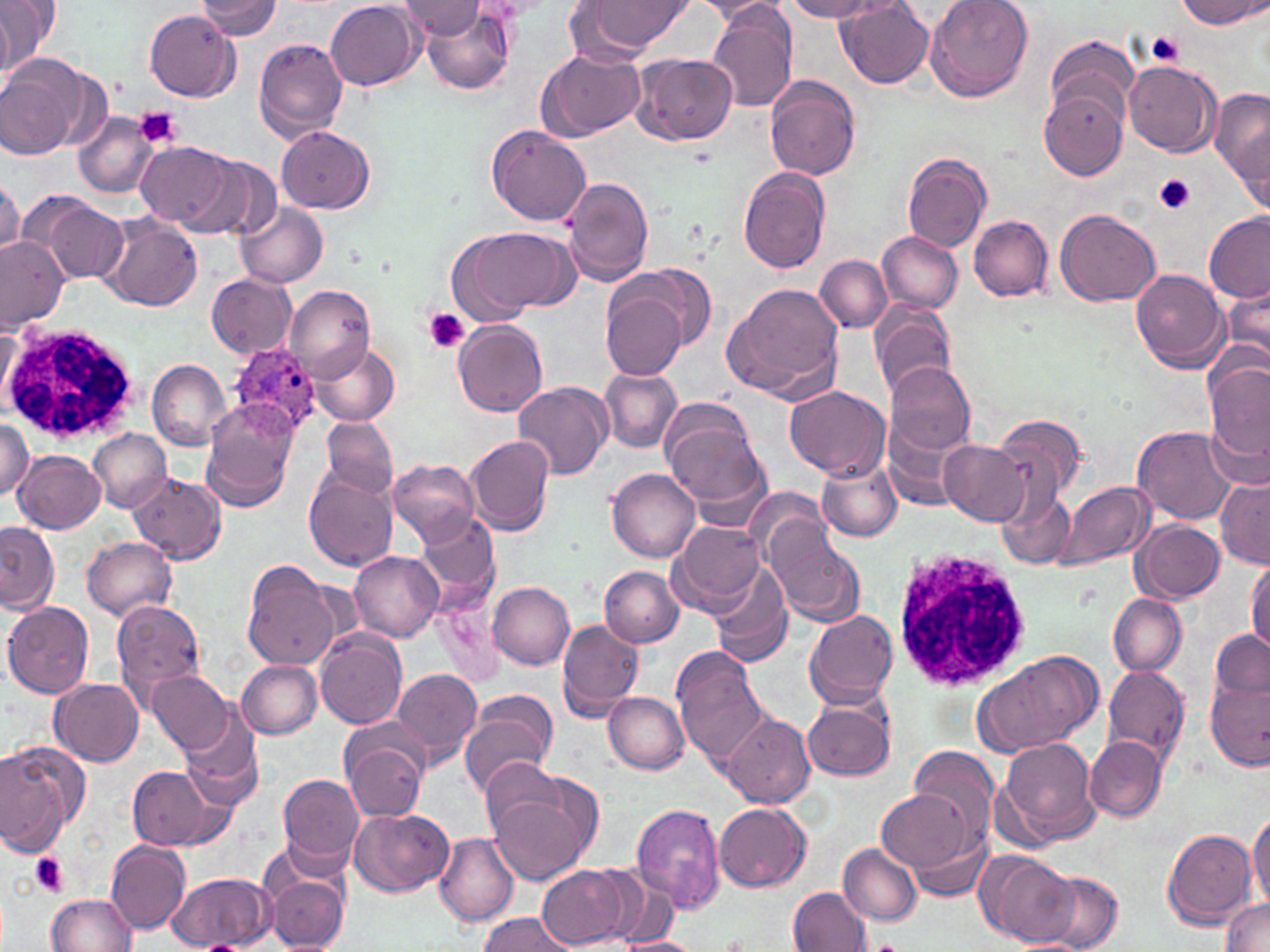

Summary:
  - Coordinate format: approximate bounding boxes as [x1, y1, x2, y2] in pixels
  - Platelet locations: [1145, 31, 1183, 68], [135, 107, 181, 150], [1154, 174, 1196, 215], [423, 308, 470, 353], [29, 852, 70, 897]
  - Plasmodium ovale-infected red blood cell locations: [226, 342, 323, 438]
  - White blood cell locations: [0, 321, 141, 444], [889, 547, 1034, 692]
  - Uninfected red blood cell locations: [0, 0, 58, 78], [196, 0, 282, 39], [325, 0, 421, 89], [586, 0, 694, 53], [693, 0, 787, 24], [784, 0, 887, 21], [835, 0, 935, 88], [925, 0, 1033, 102], [1176, 0, 1267, 30], [400, 1, 485, 39], [420, 5, 513, 96], [707, 5, 798, 114], [145, 11, 240, 101], [1043, 35, 1138, 126], [253, 37, 348, 144], [536, 49, 645, 141], [632, 52, 738, 145], [1, 56, 84, 158], [1124, 60, 1220, 157], [766, 75, 861, 179], [1212, 85, 1270, 197], [1039, 86, 1128, 180], [73, 111, 158, 198], [487, 125, 592, 227], [277, 127, 375, 213], [137, 141, 237, 231], [901, 153, 991, 252], [198, 156, 283, 241], [738, 166, 831, 274], [562, 175, 655, 287], [0, 179, 23, 259], [33, 196, 127, 284], [235, 203, 327, 289], [1055, 208, 1161, 307], [1202, 212, 1269, 304], [100, 215, 203, 310], [969, 215, 1053, 301], [451, 228, 558, 326], [878, 230, 962, 314], [0, 238, 69, 328], [816, 255, 891, 331], [636, 263, 714, 350], [1132, 269, 1228, 374], [206, 273, 296, 358], [723, 282, 847, 400], [283, 285, 374, 383], [601, 285, 688, 381], [1219, 285, 1270, 374], [869, 300, 957, 402], [454, 319, 548, 419], [0, 325, 19, 411], [310, 342, 400, 426], [146, 359, 230, 450], [884, 361, 976, 455], [1204, 361, 1270, 465], [600, 369, 682, 453], [513, 382, 613, 483], [785, 385, 889, 480], [660, 398, 764, 511], [202, 410, 294, 512], [884, 412, 970, 511], [991, 413, 1086, 504], [318, 415, 400, 501], [0, 417, 35, 498], [1131, 425, 1239, 525], [89, 429, 172, 513], [0, 432, 69, 525], [465, 435, 555, 535], [939, 439, 1031, 526], [13, 450, 104, 532], [817, 458, 902, 543], [388, 460, 483, 547], [608, 468, 701, 562], [304, 471, 398, 571], [131, 472, 226, 565], [1216, 478, 1269, 568], [1057, 481, 1153, 570], [996, 487, 1074, 570], [747, 488, 830, 562], [414, 513, 500, 607], [764, 519, 865, 627], [1132, 519, 1225, 603], [0, 521, 57, 612], [669, 521, 766, 618], [83, 537, 178, 619], [349, 551, 445, 642], [1245, 558, 1270, 654], [242, 560, 340, 670], [710, 563, 792, 668], [601, 566, 684, 647], [488, 582, 575, 668], [1109, 594, 1186, 676], [111, 598, 208, 710], [3, 602, 94, 699], [805, 609, 898, 709], [556, 619, 643, 722], [315, 627, 406, 728], [1209, 630, 1268, 704], [974, 650, 1099, 757], [674, 653, 769, 761], [236, 660, 323, 738], [1102, 664, 1190, 763], [388, 666, 480, 769], [149, 670, 235, 756], [51, 679, 144, 767], [1204, 682, 1268, 769], [603, 691, 688, 774], [460, 694, 558, 797], [802, 695, 896, 782], [177, 698, 261, 806], [721, 712, 815, 807], [344, 731, 428, 822], [1085, 736, 1167, 822], [1000, 737, 1098, 842], [0, 745, 79, 853], [909, 746, 1001, 845], [479, 758, 565, 838], [126, 764, 231, 852], [276, 773, 364, 869], [876, 790, 976, 874], [490, 793, 591, 887], [631, 804, 726, 913], [714, 804, 810, 892], [349, 807, 453, 896], [1247, 810, 1269, 906], [901, 823, 993, 901], [1161, 828, 1259, 930], [432, 832, 518, 927], [106, 840, 191, 934], [838, 843, 921, 925], [977, 852, 1076, 946], [539, 864, 632, 948], [582, 866, 672, 944], [262, 868, 350, 952], [169, 871, 274, 951], [1038, 871, 1123, 951], [790, 886, 871, 952], [45, 893, 138, 951], [1220, 898, 1270, 951], [478, 913, 575, 952], [612, 937, 701, 952]
  - Slide-level diagnosis: Plasmodium ovale
  - Preparation: thin blood film
  - Field of view: single
  - Stain: May-Grünwald-Giemsa
  - Image size: 1270×952 pixels
  - Modality: light microscopy
  - Magnification: 1000x